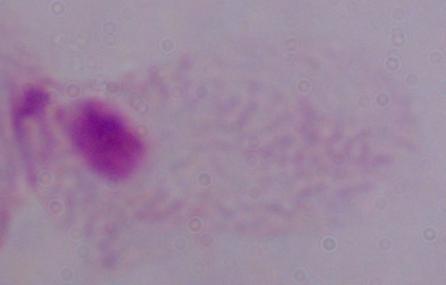
Summary:
  - Identification: trichomonad
  - Modality: photomicrograph
  - Magnification: 1000x